Assess this cell for malaria.
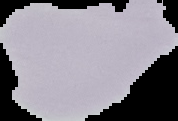
It is uninfected.

image_size: 178×121 pixels
image_type: segmented cell region with the area outside set to black
preparation: thin blood film